Classify this cell by malaria status.
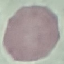
It is uninfected.

Automatically extracted cell patch, resized to 64 × 64 pixels. Photographed with a smartphone camera at the microscope eyepiece. Thin smear of blood. Giemsa-stained preparation.